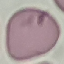
Malaria status: uninfected. Thin smear of blood. Giemsa-stained preparation. Cell patch, automatically extracted from a larger field of view and resized to 64 × 64 pixels. Acquired by smartphone through the microscope eyepiece.